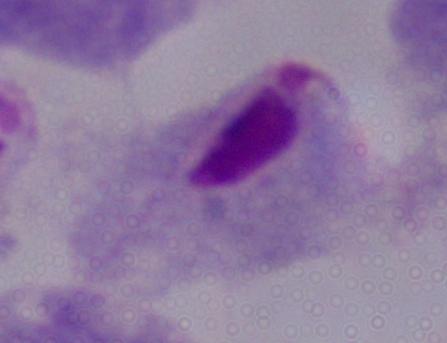

Summary:
  - Identification: trichomonad
  - Magnification: 1000x
  - Modality: photomicrograph